Report the malaria status of this cell.
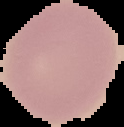

Uninfected.

Summary:
  - Image type: segmented cell region on a black background
  - Preparation: thin blood smear
  - Image size: 124×127 pixels